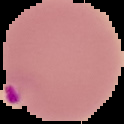
Summary:
  - Image size: 124×124 pixels
  - Malaria status: parasitized
  - Image type: cell region segmented out of the field of view; surrounding area masked to black
  - Preparation: thin blood smear